Describe the morphology of the erythrocytes.
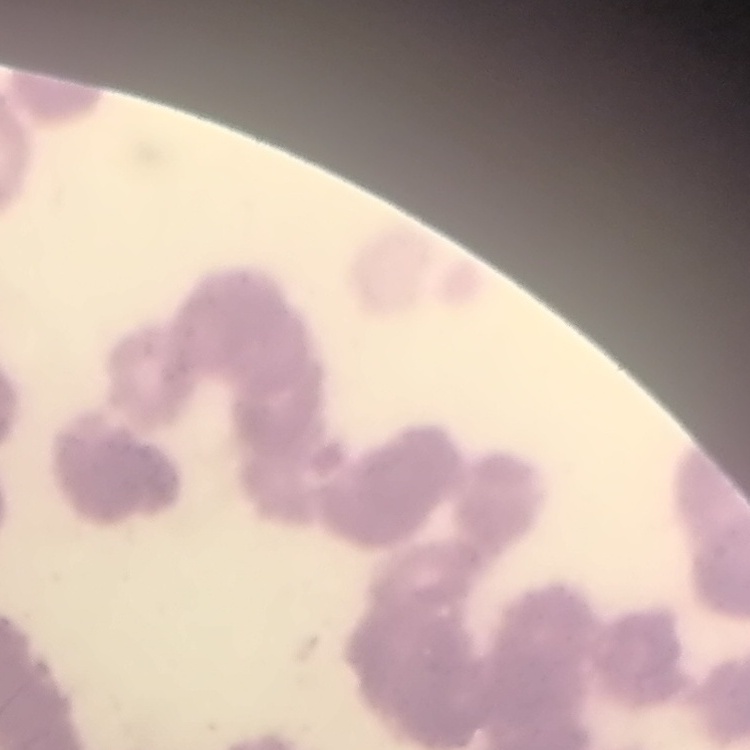
Rouleaux formation.

Thin blood film. Stained with either Field's or Giemsa. Square crop of a larger photomicrograph.